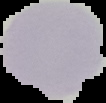
image type = segmented cell region with the area outside set to black
malaria status = uninfected
preparation = thin blood film
image size = 106×103 pixels